Identify the cell.
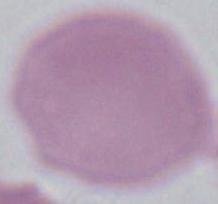

This is an erythrocyte.

Summary:
  - Modality: photomicrograph
  - Magnification: 1000x